Locate every blood parasite and identify its species.
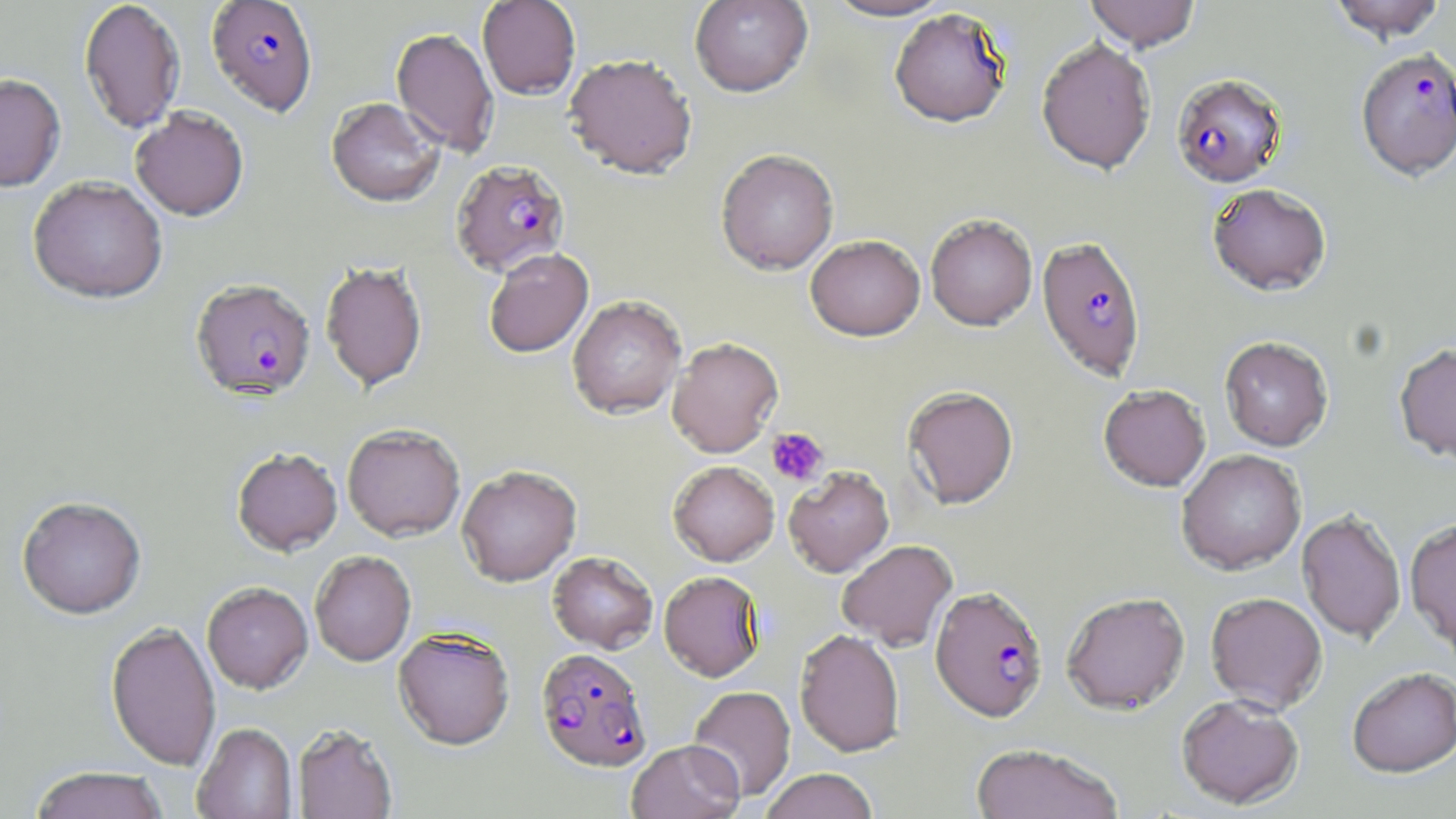
Approximate bounding boxes as (x1,y1)-(x2,y2) corner pairs in pixels.
Plasmodium falciparum-infected red blood cells: (206,0)-(318,119), (1355,48)-(1456,180), (1171,73)-(1287,187), (452,160)-(570,276), (1037,236)-(1146,382), (190,281)-(315,405), (930,585)-(1048,722), (535,648)-(652,773).
No Plasmodium ovale, Plasmodium malariae, Plasmodium vivax, Babesia divergens, or Trypanosoma brucei observed.

Summary:
  - Uninfected red blood cell locations: (78,0)-(186,135), (477,0)-(581,100), (689,0)-(813,98), (822,0)-(956,22), (1084,0)-(1201,51), (1326,0)-(1448,42), (889,8)-(1013,129), (391,27)-(499,158), (1036,37)-(1157,174), (563,55)-(698,181), (0,74)-(66,193), (326,98)-(445,209), (130,108)-(249,222), (715,149)-(839,276), (27,176)-(168,306), (1207,183)-(1332,296), (925,214)-(1037,330), (805,235)-(925,341), (484,250)-(594,360), (320,261)-(428,394), (568,298)-(686,420), (1219,336)-(1334,451), (667,338)-(783,458), (1394,343)-(1456,464), (1098,384)-(1211,491), (902,386)-(1019,509), (342,426)-(465,543), (232,449)-(343,559), (1176,449)-(1306,575), (668,461)-(779,567), (456,466)-(582,588), (784,467)-(895,578), (17,498)-(146,621), (1297,510)-(1406,644), (1405,519)-(1456,655), (837,540)-(958,652), (310,552)-(416,667), (547,552)-(658,654), (658,571)-(765,683), (202,584)-(313,695), (1061,591)-(1190,715), (1205,592)-(1327,713), (105,622)-(221,772), (393,629)-(515,751), (794,629)-(904,758), (1346,668)-(1456,779), (688,685)-(796,802), (1176,695)-(1304,810), (192,724)-(297,819), (293,725)-(398,819), (627,740)-(744,819), (970,743)-(1124,819), (28,767)-(170,819), (759,769)-(878,819)
  - Platelet locations: (766,427)-(828,485)
  - Slide-level diagnosis: Plasmodium falciparum
  - Stain: May-Grünwald-Giemsa
  - Magnification: 1000x
  - Image size: 1456×819 pixels
  - Field of view: single
  - Preparation: thin blood film
  - Modality: light microscopy